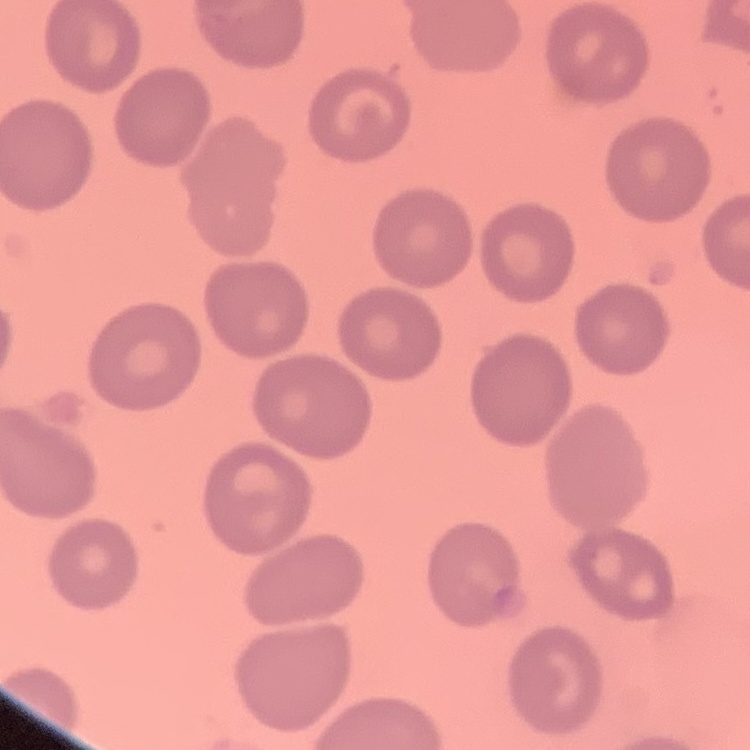 The erythrocytes exhibit no rouleaux formation. Thin peripheral smear. Square crop of a larger photomicrograph. Field's or Giemsa stain.